Assess this cell for malaria.
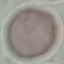

Uninfected.

Automatically extracted cell patch, resized to 64 × 64 pixels. Thin blood film. Acquired by smartphone through the microscope eyepiece. Giemsa stain.